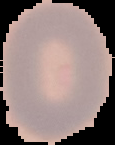

Summary:
  - Image size: 115×145 pixels
  - Preparation: thin blood film
  - Image type: segmented cell region with the area outside set to black
  - Malaria status: uninfected